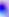
Summary:
  - Modality: photomicrograph
  - Magnification: 400x
  - Identification: Toxoplasma gondii